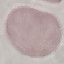
Malaria status: uninfected. Automatically extracted cell patch, resized to 64 × 64 pixels. Photographed with a smartphone camera at the microscope eyepiece. Thin smear of blood. Giemsa stain.